State which parasite is depicted.
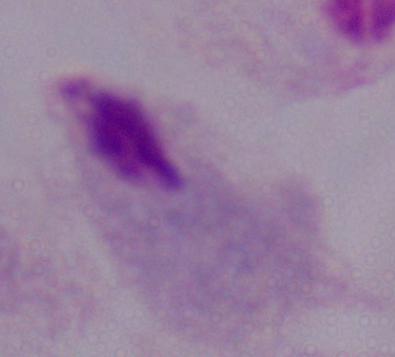

A trichomonad.

Captured at 1000x magnification. Micrograph.